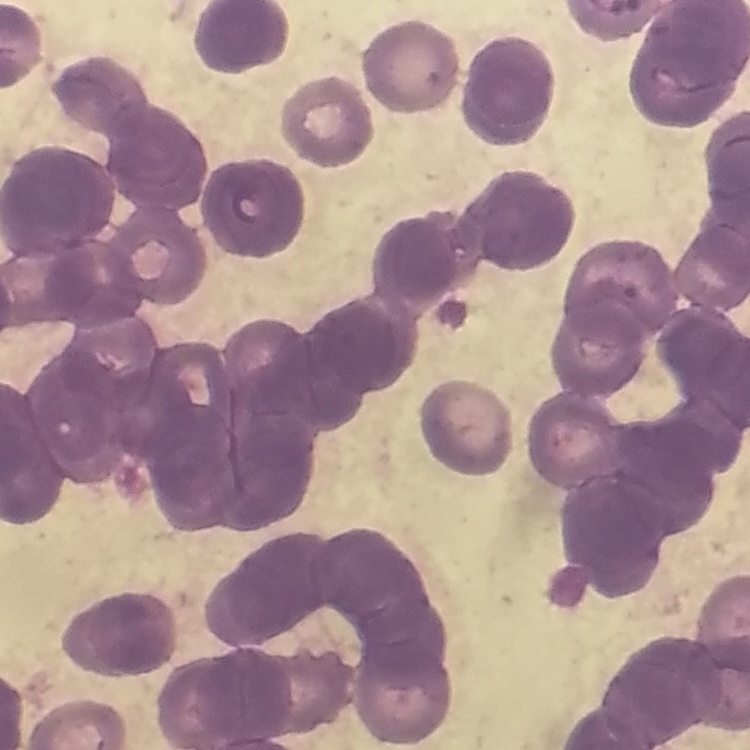

red blood cell morphology = rouleaux formation
image type = one tile cut from a larger photomicrograph
stain = Field's or Giemsa
preparation = thin blood film